Comment on the morphology of the erythrocytes.
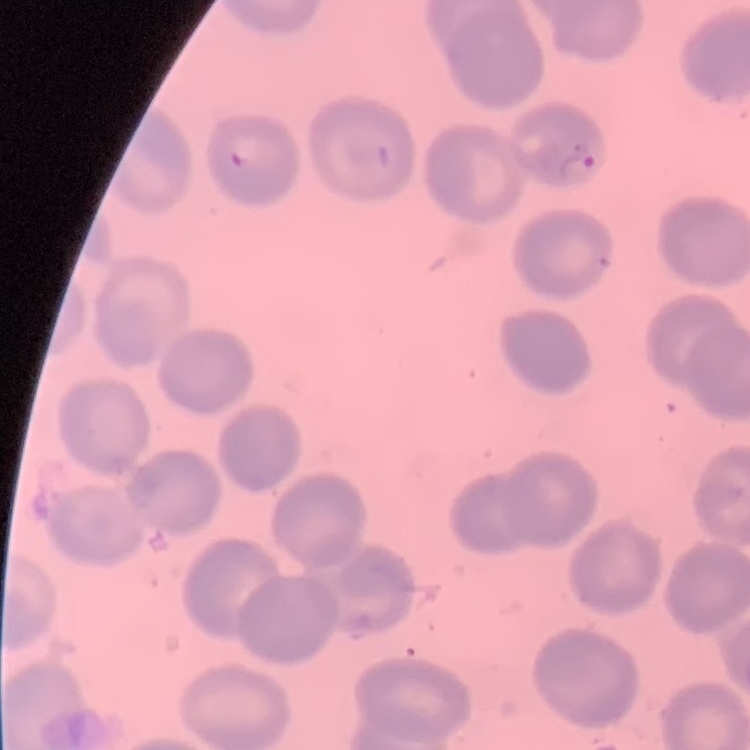
No rouleaux formation.

preparation: thin blood smear
image_type: square crop of a larger photomicrograph
stain: Field's or Giemsa